Identify the parasite.
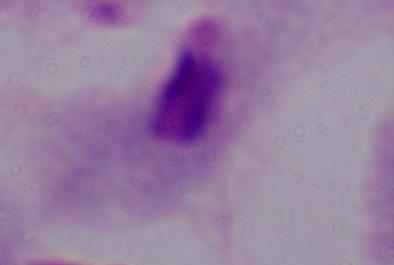
A trichomonad.

modality = photomicrograph
magnification = 1000x